Identify the cell.
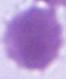

This is an erythrocyte.

Captured at 1000x magnification. Photomicrograph.